Describe the morphology of the erythrocytes.
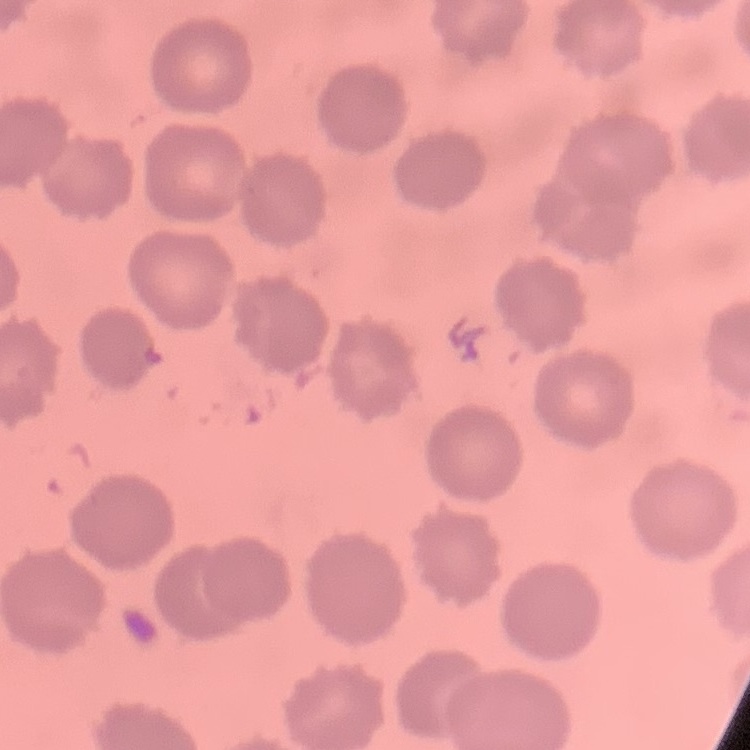
They show no rouleaux formation.

Summary:
  - Stain: Field's or Giemsa
  - Preparation: thin blood smear
  - Image type: one tile cut from a larger photomicrograph